State which cell type is depicted.
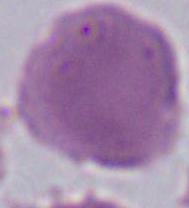
An erythrocyte.

magnification = 1000x
modality = photomicrograph